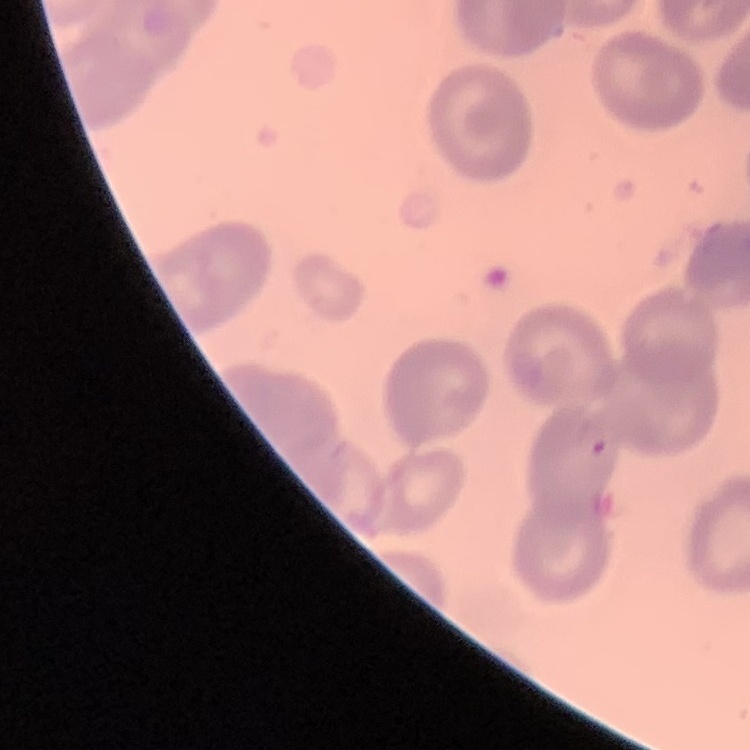

Summary:
  - Erythrocyte morphology: no rouleaux formation
  - Preparation: thin blood film
  - Stain: Field's or Giemsa
  - Image type: one tile cut from a larger photomicrograph